Identify the parasite.
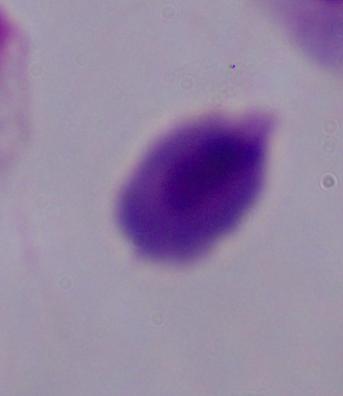

A trichomonad.

magnification: 1000x
modality: micrograph